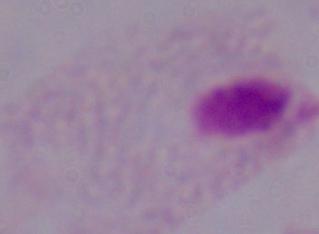
modality = micrograph
magnification = 1000x
identification = trichomonad